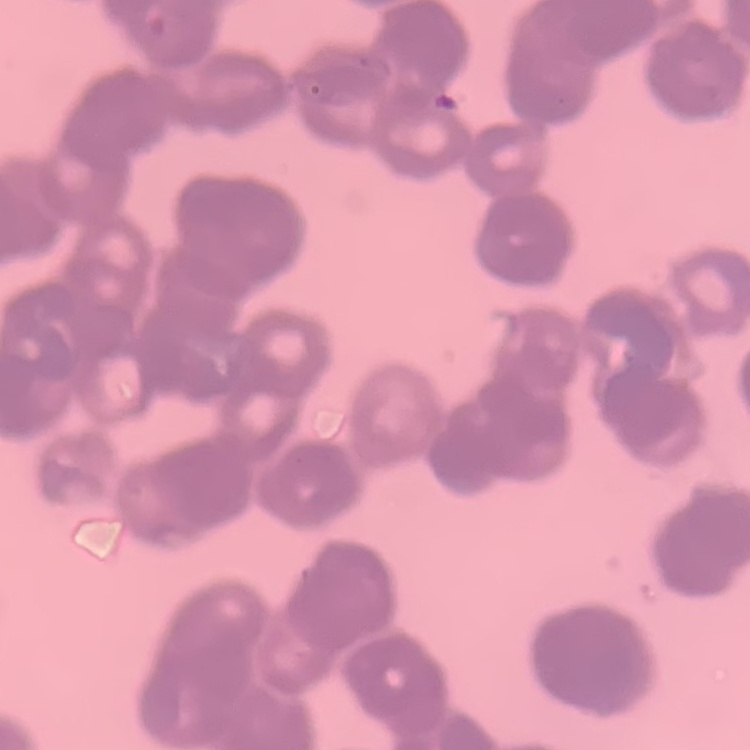 The red blood cells show rouleaux formation. Stained with either Field's or Giemsa. One tile cut from a larger photomicrograph. Thin blood film.